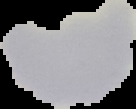

Summary:
  - Result: no malaria parasites seen
  - Image size: 136×109 pixels
  - Image type: cell region segmented out of the field of view; surrounding area masked to black
  - Preparation: thin blood smear